Report the malaria status of this cell.
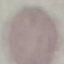
It is uninfected.

Thin blood smear. Giemsa stain. Automatically extracted cell patch, resized to 64 × 64 pixels. Photographed with a smartphone camera at the microscope eyepiece.